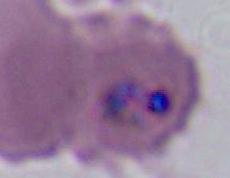
Summary:
  - Identification: Plasmodium
  - Modality: photomicrograph
  - Magnification: 400x or 1000x